Comment on the morphology of the erythrocytes.
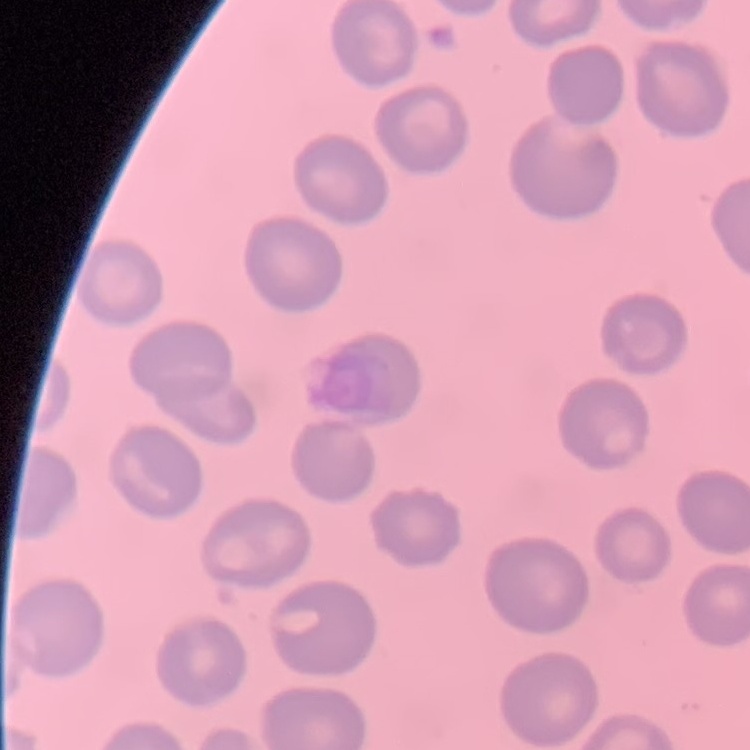
They show no rouleaux formation.

{
  "stain": "Field's or Giemsa",
  "preparation": "thin blood smear",
  "image_type": "one tile cut from a larger photomicrograph"
}